Locate every blood parasite and identify its species.
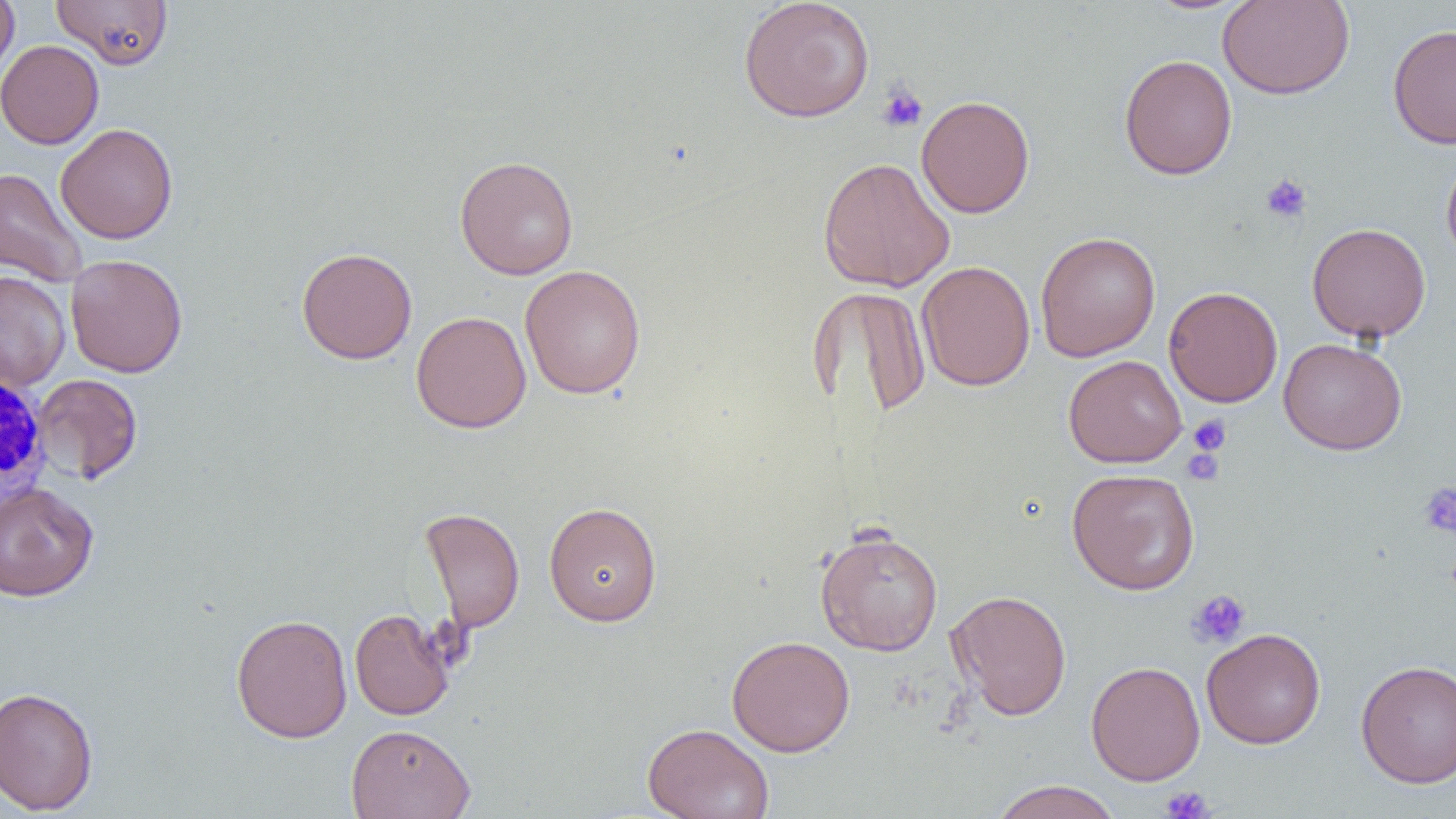
No blood parasites observed.

Summary:
  - Coordinate format: approximate bounding boxes as (x1, y1, x2, y2) in pixels
  - White blood cell locations: (1, 370, 51, 507)
  - Uninfected red blood cell locations: (0, 0, 19, 83), (51, 0, 173, 69), (738, 0, 875, 123), (1217, 0, 1355, 100), (1387, 23, 1456, 149), (0, 40, 104, 149), (1119, 53, 1238, 180), (916, 95, 1035, 218), (55, 123, 179, 244), (1441, 153, 1456, 268), (455, 155, 579, 280), (817, 156, 955, 293), (0, 167, 88, 288), (1306, 222, 1431, 342), (1034, 231, 1161, 361), (296, 247, 417, 364), (65, 254, 188, 378), (916, 260, 1035, 391), (519, 265, 646, 399), (0, 270, 70, 391), (1164, 286, 1283, 408), (811, 288, 933, 419), (411, 310, 531, 434), (1279, 337, 1407, 455), (1063, 355, 1187, 468), (32, 373, 143, 484), (1066, 467, 1200, 595), (0, 482, 99, 602), (544, 501, 662, 626), (420, 507, 525, 633), (814, 526, 944, 655), (947, 590, 1071, 720), (349, 608, 455, 720), (230, 613, 353, 743), (1201, 627, 1327, 749), (726, 635, 855, 757), (1355, 659, 1456, 788), (1086, 660, 1205, 786), (0, 686, 99, 815), (642, 722, 774, 819), (345, 724, 476, 819), (988, 780, 1124, 819)
  - Platelet locations: (877, 84, 928, 133), (1261, 173, 1311, 223), (1188, 415, 1231, 456), (1182, 442, 1226, 487), (1418, 481, 1456, 538), (1187, 589, 1251, 649), (1160, 785, 1214, 818)
  - Slide-level diagnosis: negative for blood parasites
  - Field of view: single
  - Modality: optical microscopy
  - Magnification: 1000x
  - Image size: 1456×819 pixels
  - Preparation: thin blood film